Name the blood parasite species.
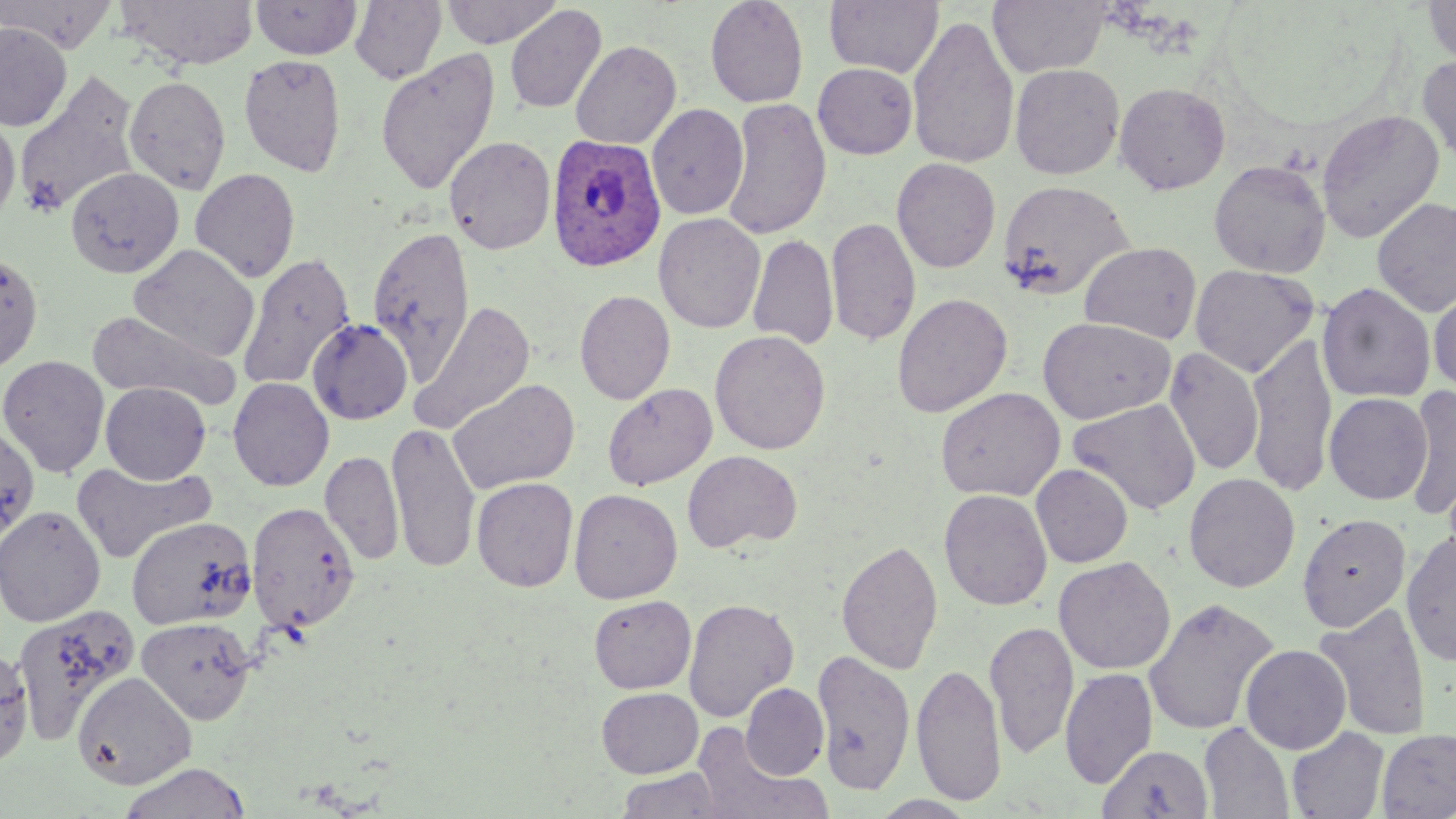

Plasmodium ovale.

image size = 1456×819 pixels
field of view = single
Plasmodium ovale-infected red blood cell locations = approximate bounding boxes as [x1, y1, x2, y2] in pixels: [547, 134, 666, 273]
preparation = thin blood smear
magnification = 1000x
uninfected red blood cell locations = approximate bounding boxes as [x1, y1, x2, y2] in pixels: [0, 0, 119, 52], [116, 0, 259, 70], [251, 0, 362, 60], [349, 0, 447, 85], [441, 0, 562, 48], [705, 0, 809, 108], [824, 0, 944, 79], [987, 0, 1110, 77], [1422, 0, 1456, 67], [504, 5, 607, 114], [907, 15, 1020, 171], [0, 23, 72, 131], [570, 40, 681, 150], [375, 48, 501, 197], [239, 53, 348, 176], [1417, 54, 1456, 165], [813, 62, 918, 159], [1010, 63, 1125, 180], [14, 71, 143, 217], [124, 75, 231, 195], [1114, 81, 1231, 195], [722, 97, 832, 241], [646, 103, 748, 220], [1316, 109, 1445, 243], [0, 112, 20, 224], [444, 135, 556, 255], [891, 158, 1000, 273], [1209, 160, 1331, 277], [65, 167, 184, 279], [190, 168, 301, 283], [998, 179, 1135, 300], [1372, 196, 1456, 318], [653, 213, 765, 333], [826, 216, 921, 346], [368, 224, 476, 383], [747, 235, 838, 352], [1079, 242, 1202, 345], [128, 244, 259, 362], [0, 250, 43, 374], [237, 251, 355, 391], [1189, 263, 1319, 378], [1317, 282, 1436, 404], [1429, 282, 1456, 396], [574, 289, 675, 405], [892, 292, 1013, 418], [412, 301, 536, 434], [87, 308, 244, 410], [1037, 315, 1175, 425], [307, 318, 413, 425], [710, 330, 831, 455], [1246, 331, 1337, 499], [1164, 346, 1264, 477], [0, 354, 110, 478], [227, 376, 334, 491], [448, 378, 581, 495], [100, 382, 211, 484], [602, 383, 717, 491], [1402, 386, 1455, 520], [936, 387, 1066, 501], [1324, 392, 1432, 504], [1067, 398, 1201, 515], [387, 419, 481, 575], [0, 424, 40, 546], [320, 450, 404, 566], [683, 450, 802, 554], [71, 460, 215, 564], [1031, 464, 1133, 567], [1184, 472, 1301, 593], [471, 477, 579, 592], [569, 488, 683, 603], [939, 489, 1052, 611], [246, 501, 360, 633], [0, 505, 106, 626], [1297, 513, 1411, 632], [126, 516, 256, 629], [1401, 531, 1456, 667], [836, 538, 943, 676], [1054, 556, 1175, 675], [588, 595, 696, 693], [1143, 596, 1280, 736], [684, 598, 798, 722], [1314, 601, 1433, 740], [10, 605, 139, 748], [136, 616, 257, 724], [985, 620, 1079, 760], [1240, 644, 1351, 754], [1, 645, 34, 771], [814, 646, 915, 796], [911, 662, 1006, 806], [1060, 668, 1157, 789], [73, 672, 196, 789], [741, 683, 828, 779], [596, 687, 703, 778], [1199, 721, 1295, 819], [691, 723, 829, 819], [1286, 727, 1390, 819], [1376, 729, 1456, 818], [1098, 744, 1213, 819], [116, 761, 254, 819], [614, 767, 728, 819], [869, 795, 979, 818]
stain = May-Grünwald-Giemsa
modality = optical microscopy